Comment on the morphology of the erythrocytes.
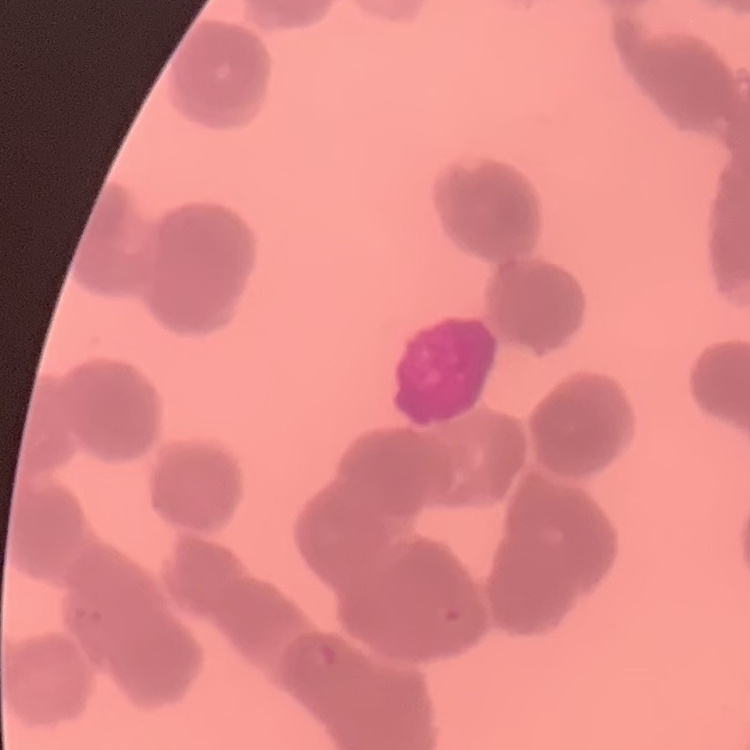

They show rouleaux formation.

Summary:
  - Image type: square crop of a larger photomicrograph
  - Stain: Field's or Giemsa
  - Preparation: thin blood smear